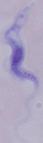

Summary:
  - Modality: photomicrograph
  - Identification: trypanosome
  - Magnification: 1000x